Identify the parasite.
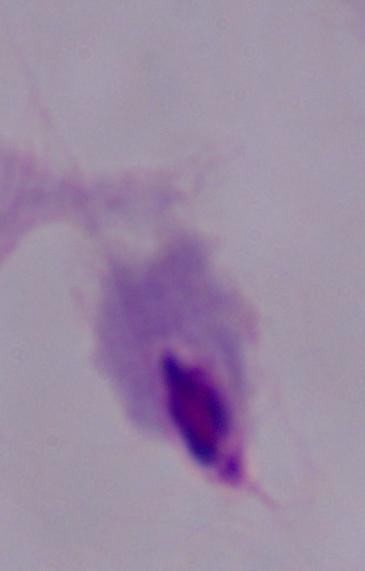

This is a trichomonad.

Summary:
  - Modality: micrograph
  - Magnification: 1000x